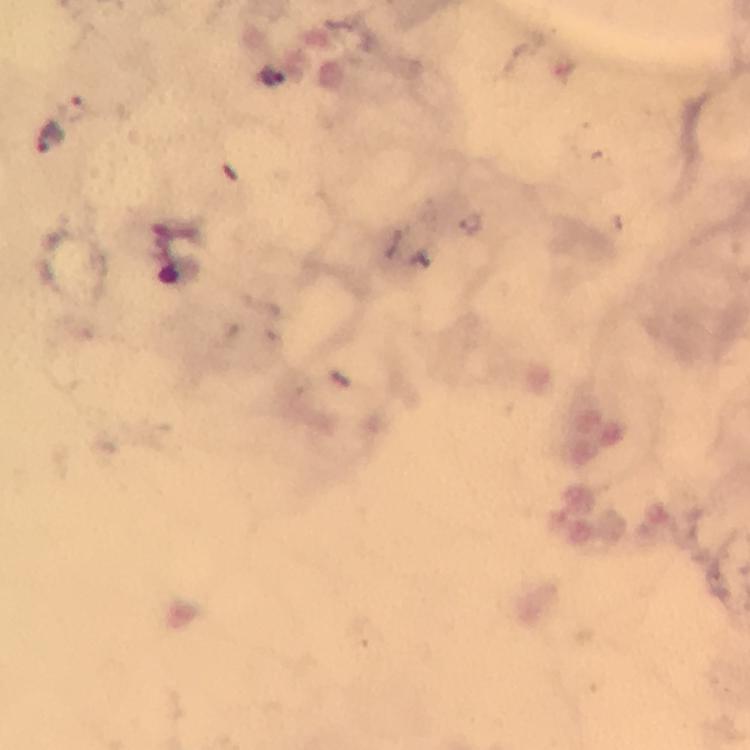
Approximate object centers, in pixels from the top-left corner. Plasmodium parasite locations: (x=270, y=76), (x=48, y=137). Thick blood smear. At 100x magnification. Immersion oil was used. Giemsa stain. Photographed through the microscope with a smartphone camera. Image is 750×750 pixels. Cropped region of a single field of view. From a diagnostic examination for malaria.